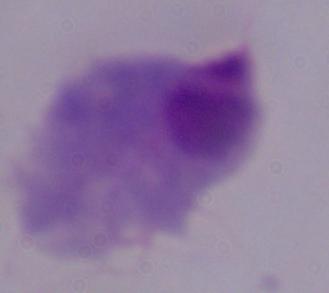

Summary:
  - Identification: trichomonad
  - Magnification: 1000x
  - Modality: micrograph